Locate and identify every blood parasite.
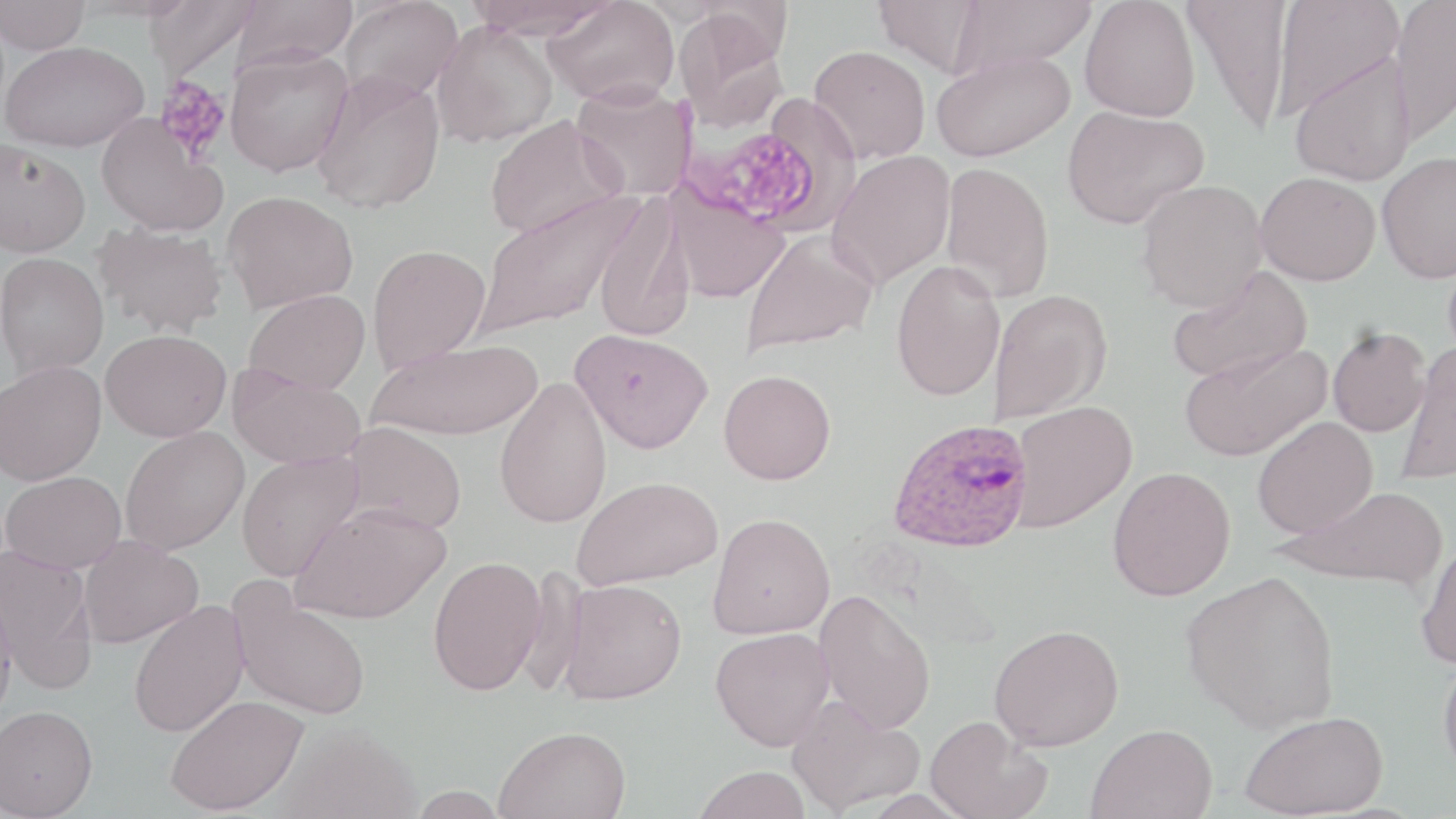
Approximate bounding boxes as (x1,y1)-(x2,y2) corner pairs in pixels.
Plasmodium ovale-infected red blood cells: (886,417)-(1034,553).
No Plasmodium falciparum, Plasmodium malariae, Plasmodium vivax, Babesia divergens, or Trypanosoma brucei observed.

Uninfected red blood cell locations: (0,0)-(91,54), (145,0)-(261,81), (233,0)-(360,70), (338,0)-(463,106), (463,0)-(617,39), (543,0)-(680,108), (874,0)-(989,76), (951,0)-(1097,74), (1080,0)-(1201,122), (1182,0)-(1293,136), (1271,0)-(1404,120), (1389,0)-(1456,146), (672,10)-(790,130), (431,21)-(558,148), (2,40)-(149,152), (809,44)-(931,164), (224,47)-(354,176), (931,50)-(1076,163), (1288,53)-(1417,186), (311,71)-(446,214), (571,81)-(697,201), (1061,105)-(1208,229), (483,113)-(626,239), (97,114)-(228,236), (0,139)-(90,257), (826,150)-(956,289), (1377,150)-(1456,284), (940,162)-(1054,301), (1255,171)-(1381,285), (1136,179)-(1268,312), (666,186)-(789,303), (223,190)-(358,312), (475,190)-(642,337), (592,196)-(695,343), (93,221)-(229,339), (741,230)-(878,356), (366,244)-(491,373), (0,252)-(108,378), (891,259)-(1006,402), (1166,265)-(1313,386), (988,288)-(1112,425), (243,289)-(371,395), (1327,326)-(1430,437), (570,328)-(714,453), (100,329)-(231,442), (368,340)-(542,441), (1179,341)-(1332,461), (1397,342)-(1456,485), (0,360)-(107,485), (227,364)-(366,470), (719,369)-(836,484), (494,377)-(613,528), (1008,399)-(1138,533), (1252,416)-(1378,538), (341,422)-(467,534), (119,426)-(249,555), (236,451)-(364,580), (1107,466)-(1236,601), (1,471)-(127,574), (573,475)-(723,589), (1283,486)-(1448,590), (290,501)-(450,624), (708,512)-(835,639), (78,535)-(203,648), (1415,538)-(1456,670), (0,544)-(98,693), (428,555)-(547,695), (1181,569)-(1341,733), (557,578)-(687,705), (228,580)-(371,720), (0,587)-(17,729), (814,589)-(936,735), (127,600)-(249,738), (989,623)-(1124,751), (710,626)-(835,751), (1438,651)-(1456,779), (165,694)-(309,815), (786,694)-(925,815), (0,705)-(98,819), (1240,710)-(1388,818), (925,715)-(1051,819), (275,723)-(421,819), (1086,723)-(1218,819), (494,725)-(631,819), (692,765)-(812,819). Platelet locations: (155,76)-(232,162), (681,116)-(831,229). Slide-level diagnosis: Plasmodium ovale. Single field of view. Image is 1456×819 pixels. Light microscopy. 1000x magnification. May-Grünwald-Giemsa-stained preparation. Thin blood smear.